Outline each blood parasite and name the species.
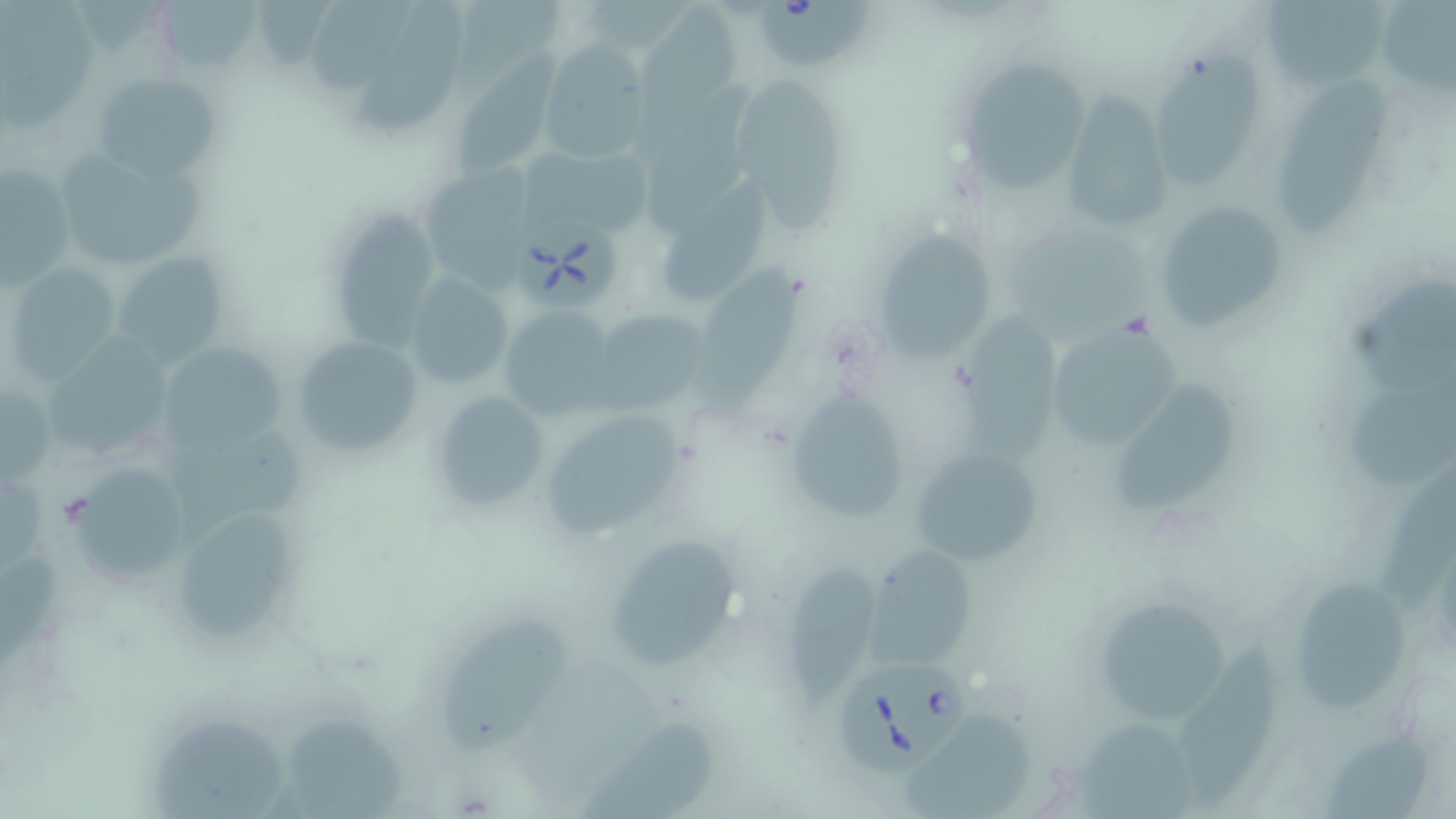
Approximate bounding boxes as named x1/y1/x2/y2 corners in pixels.
Babesia divergens-infected red blood cells: (x1=753, y1=0, x2=872, y2=69), (x1=514, y1=221, x2=636, y2=313), (x1=838, y1=655, x2=977, y2=772).
No Plasmodium falciparum, Plasmodium ovale, Plasmodium malariae, Plasmodium vivax, or Trypanosoma brucei observed.

slide_level_diagnosis: Babesia divergens
stain: May-Grünwald-Giemsa
field_of_view: one of a larger specimen
image_size: 1456×819 pixels
uninfected_red_blood_cell_locations: 'approximate bounding boxes as named x1/y1/x2/y2 corners in pixels: (x1=159, y1=0, x2=256, y2=71), (x1=310, y1=0, x2=414, y2=89), (x1=359, y1=0, x2=468, y2=129), (x1=1259, y1=1, x2=1389, y2=93), (x1=1379, y1=1, x2=1456, y2=94), (x1=636, y1=4, x2=741, y2=108), (x1=537, y1=42, x2=652, y2=164), (x1=1159, y1=50, x2=1267, y2=185), (x1=952, y1=55, x2=1091, y2=192), (x1=91, y1=70, x2=223, y2=185), (x1=456, y1=70, x2=553, y2=178), (x1=723, y1=72, x2=846, y2=228), (x1=1270, y1=75, x2=1396, y2=235), (x1=638, y1=80, x2=759, y2=235), (x1=1059, y1=97, x2=1173, y2=233), (x1=46, y1=142, x2=207, y2=269), (x1=541, y1=145, x2=655, y2=240), (x1=425, y1=161, x2=533, y2=290), (x1=2, y1=164, x2=77, y2=286), (x1=666, y1=184, x2=770, y2=304), (x1=1152, y1=199, x2=1289, y2=335), (x1=335, y1=215, x2=442, y2=349), (x1=876, y1=232, x2=1000, y2=358), (x1=113, y1=252, x2=228, y2=368), (x1=4, y1=263, x2=122, y2=380), (x1=698, y1=264, x2=803, y2=427), (x1=404, y1=271, x2=514, y2=390), (x1=1353, y1=275, x2=1456, y2=394), (x1=952, y1=305, x2=1062, y2=458), (x1=498, y1=306, x2=618, y2=416), (x1=590, y1=309, x2=707, y2=414), (x1=1046, y1=320, x2=1184, y2=455), (x1=53, y1=333, x2=166, y2=445), (x1=289, y1=336, x2=423, y2=461), (x1=166, y1=344, x2=281, y2=463), (x1=1343, y1=379, x2=1456, y2=488), (x1=1113, y1=383, x2=1242, y2=512), (x1=0, y1=387, x2=55, y2=485), (x1=783, y1=388, x2=915, y2=521), (x1=430, y1=389, x2=555, y2=516), (x1=537, y1=409, x2=686, y2=543), (x1=908, y1=447, x2=1041, y2=567), (x1=74, y1=470, x2=190, y2=581), (x1=1388, y1=474, x2=1456, y2=604), (x1=183, y1=505, x2=301, y2=643), (x1=600, y1=535, x2=745, y2=673), (x1=863, y1=546, x2=976, y2=672), (x1=787, y1=559, x2=885, y2=712), (x1=1296, y1=581, x2=1407, y2=713), (x1=1090, y1=594, x2=1236, y2=727), (x1=438, y1=610, x2=565, y2=750), (x1=1174, y1=630, x2=1285, y2=808), (x1=903, y1=710, x2=1037, y2=815), (x1=580, y1=712, x2=717, y2=819), (x1=284, y1=713, x2=404, y2=817), (x1=153, y1=720, x2=287, y2=819), (x1=1078, y1=722, x2=1200, y2=819), (x1=1326, y1=730, x2=1434, y2=819)'
preparation: thin blood smear
magnification: 1000x
modality: light microscopy